State which parasite is depicted.
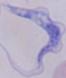
This is a trypanosome.

modality: micrograph
magnification: 1000x